Identify the blood parasite species.
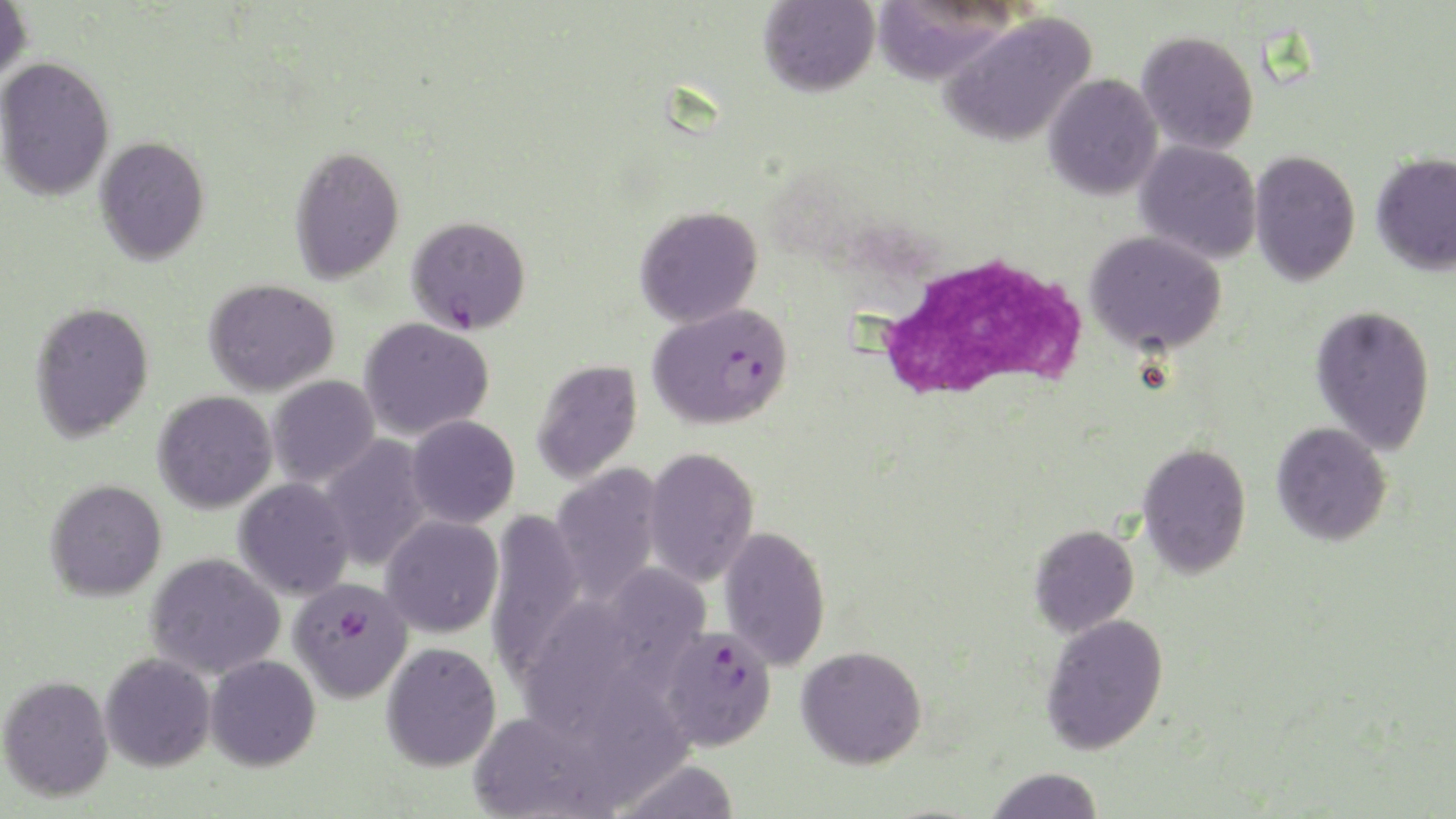
Plasmodium falciparum.

Approximate bounding boxes as [x1, y1, x2, y2] in pixels. Uninfected red blood cell locations: [0, 0, 32, 83], [759, 0, 879, 97], [871, 1, 1015, 84], [940, 12, 1096, 147], [1136, 30, 1260, 155], [0, 56, 115, 201], [1043, 74, 1163, 200], [94, 136, 210, 265], [1134, 140, 1262, 263], [288, 145, 405, 285], [1248, 149, 1361, 286], [1371, 151, 1456, 276], [635, 205, 763, 328], [1085, 230, 1227, 355], [203, 278, 339, 397], [29, 301, 154, 443], [1310, 304, 1436, 456], [358, 317, 495, 439], [530, 358, 643, 485], [267, 375, 380, 487], [152, 390, 278, 513], [406, 415, 520, 528], [1271, 422, 1392, 546], [320, 435, 434, 573], [1138, 442, 1252, 579], [643, 447, 760, 588], [550, 463, 663, 607], [233, 478, 355, 601], [44, 479, 167, 601], [487, 509, 585, 681], [380, 515, 503, 638], [1028, 524, 1139, 637], [718, 525, 831, 671], [146, 552, 285, 679], [595, 561, 711, 681], [525, 605, 660, 746], [1040, 614, 1169, 755], [382, 641, 501, 772], [795, 645, 927, 769], [100, 654, 215, 772], [204, 655, 321, 771], [595, 668, 704, 808], [0, 674, 114, 802], [468, 710, 616, 819], [614, 759, 740, 818], [985, 767, 1105, 819]. White blood cell locations: [860, 249, 1091, 408]. Plasmodium falciparum-infected red blood cell locations: [406, 215, 531, 334], [648, 302, 793, 429], [288, 576, 413, 703], [658, 625, 777, 751]. One field of a larger specimen. May-Grünwald-Giemsa stain. Thin blood film. 1000x magnification. Optical microscopy. Image is 1456×819 pixels.